Outline malaria parasites and classify them by life-cycle stage.
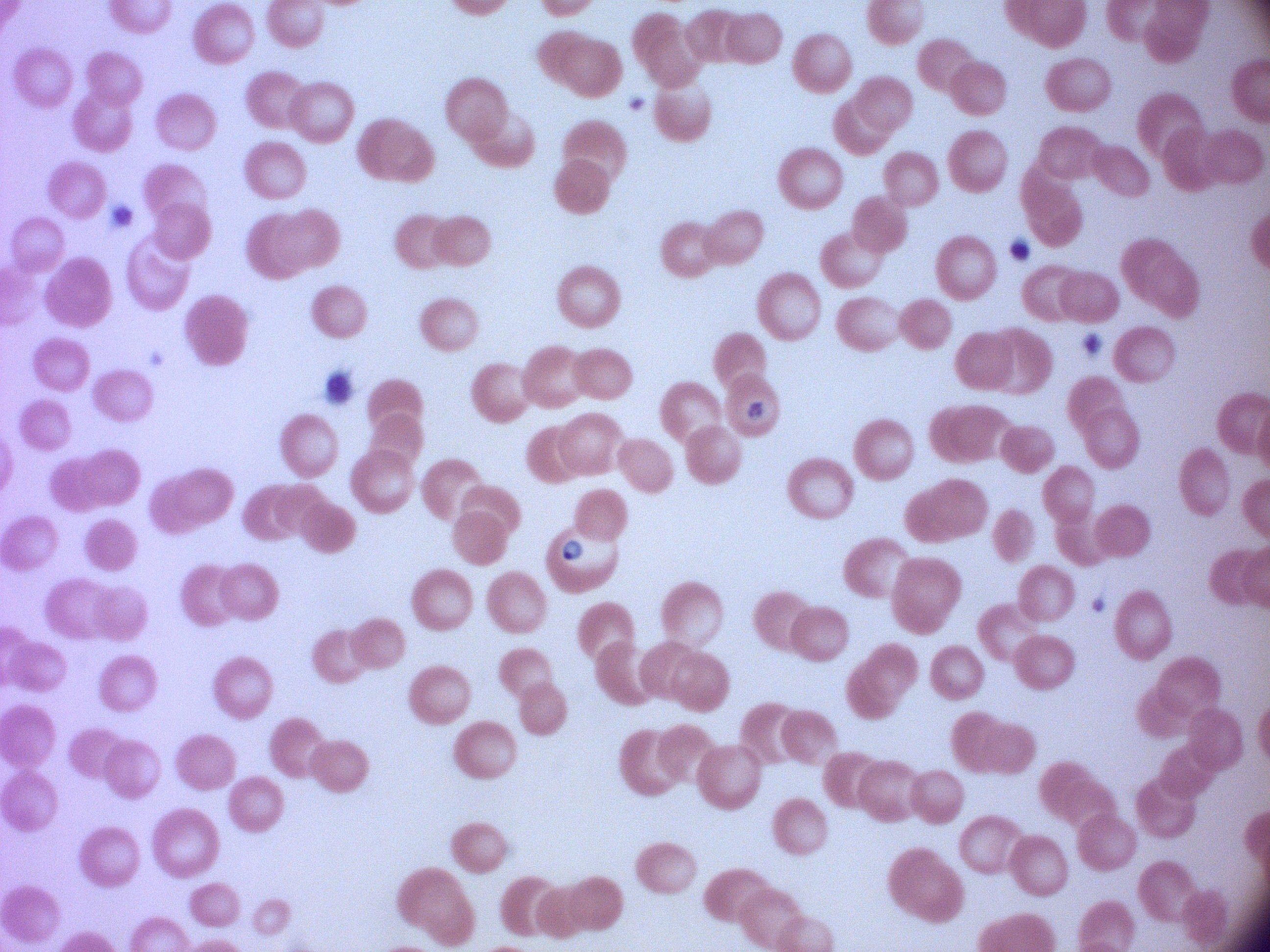
Approximate bounding boxes as named x1/y1/x2/y2 corners in pixels, from the source annotation, which is not necessarily exhaustive.
Ring forms: (x1=556, y1=532, x2=590, y2=566).

magnification: 100x
stain: Giemsa
microscope: Leica DM2000 with built-in camera
image_size: 1270×952 pixels
species: Plasmodium falciparum
field_of_view: one from this slide
preparation: thin blood film